Assess this cell for malaria.
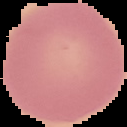
Uninfected.

From a thin blood smear. Image is 127×127 pixels. Cell region segmented out of the field of view; the surrounding area is masked to black.